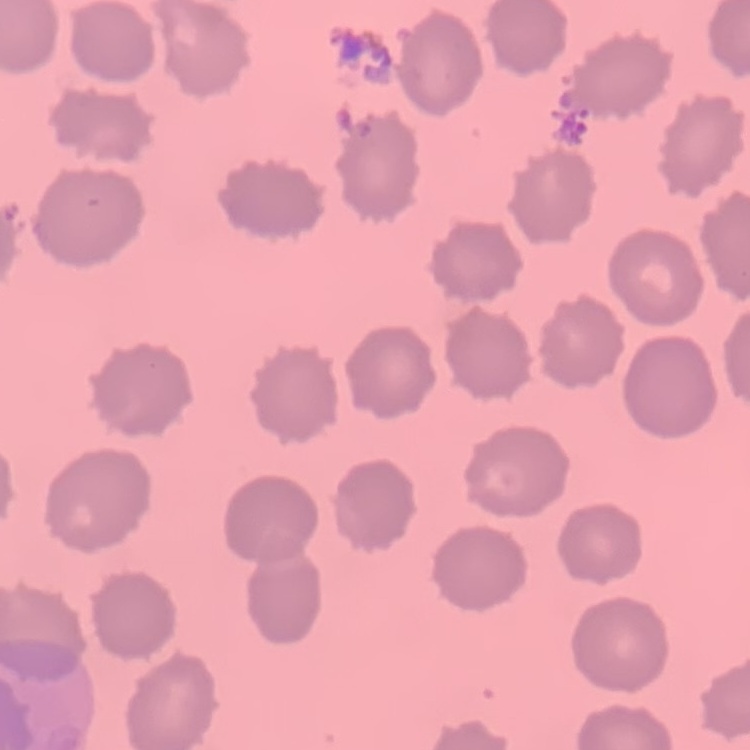
Summary:
  - Erythrocyte morphology: no rouleaux formation
  - Preparation: thin blood smear
  - Image type: square crop of a larger photomicrograph
  - Stain: Field's or Giemsa